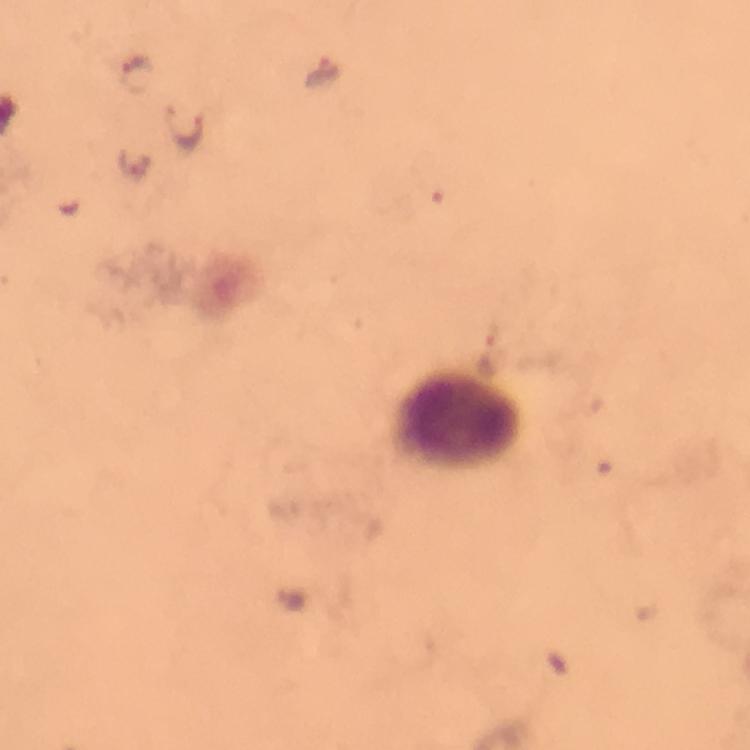
stain = Giemsa
immersion oil = applied
context = from a malaria diagnostic workup
cropped from = a single field of view
capture = smartphone camera through the microscope
leukocyte locations = approximate centers as {x, y} in pixels: {459, 424}
image size = 750×750 pixels
malaria parasite locations = approximate centers as {x, y} in pixels: {323, 72}, {135, 74}, {184, 125}, {135, 167}, {488, 356}
magnification = 100x
preparation = thick blood film